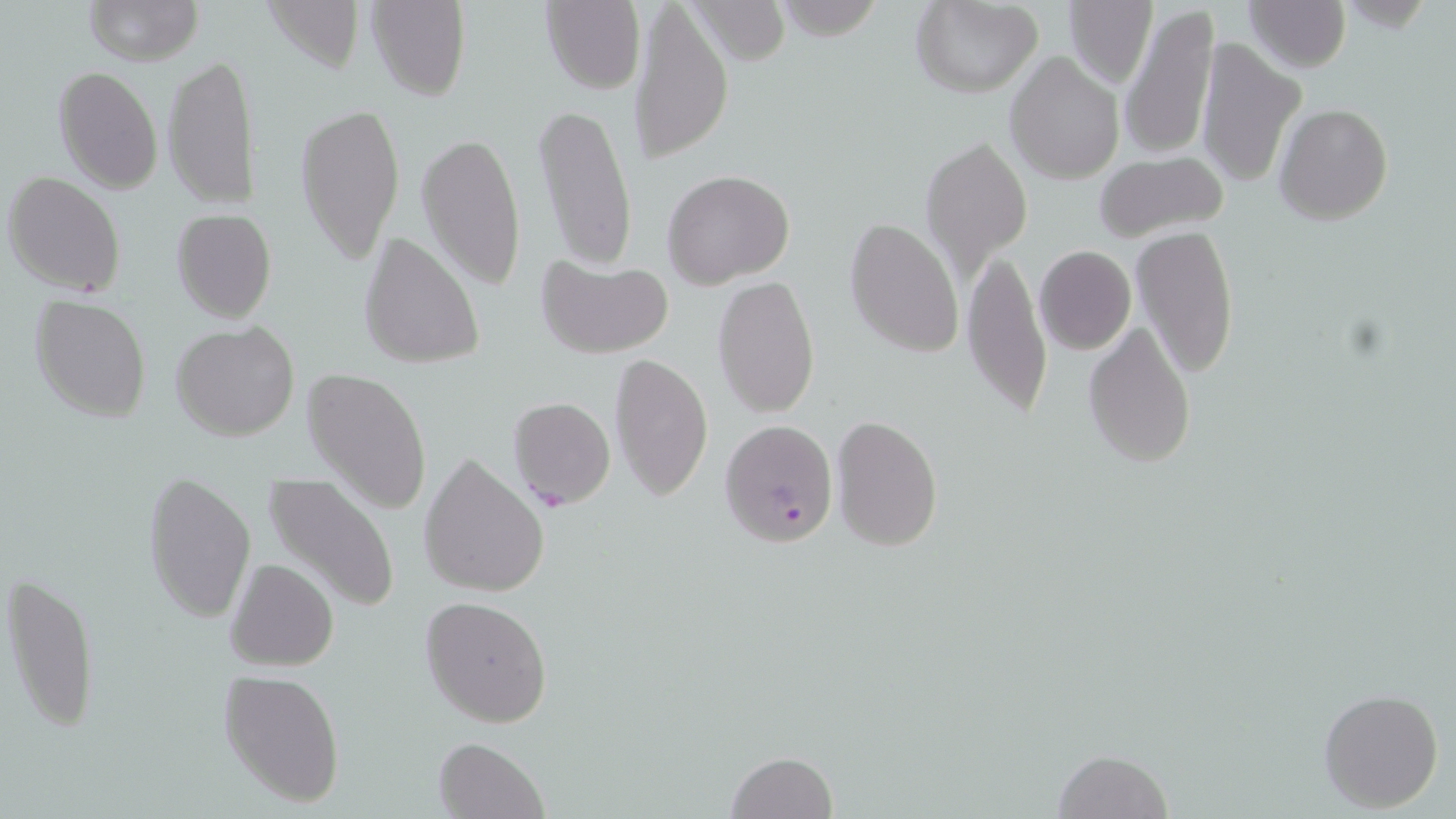
Summary:
  - Coordinate format: approximate bounding boxes as [x1, y1, x2, y2] in pixels
  - Plasmodium falciparum-infected red blood cell locations: [719, 419, 840, 549]
  - Uninfected red blood cell locations: [83, 0, 203, 66], [366, 0, 471, 101], [1063, 0, 1157, 89], [1243, 0, 1351, 72], [541, 1, 645, 95], [910, 1, 1044, 98], [1118, 2, 1219, 160], [630, 3, 734, 165], [1195, 38, 1306, 187], [1005, 50, 1125, 185], [163, 52, 261, 209], [54, 64, 162, 193], [295, 102, 405, 266], [532, 102, 638, 272], [1275, 104, 1393, 225], [415, 129, 528, 291], [922, 133, 1032, 285], [1092, 152, 1231, 246], [662, 170, 796, 288], [5, 171, 125, 296], [171, 208, 277, 323], [845, 217, 963, 358], [1131, 223, 1240, 379], [358, 230, 485, 371], [1034, 246, 1136, 354], [961, 247, 1052, 421], [535, 254, 674, 359], [712, 273, 820, 419], [31, 295, 152, 422], [171, 320, 299, 441], [1082, 321, 1196, 470], [610, 353, 713, 501], [303, 368, 433, 515], [507, 396, 616, 511], [831, 414, 943, 550], [418, 456, 550, 598], [142, 471, 257, 625], [262, 471, 400, 614], [227, 557, 339, 672], [5, 569, 99, 740], [421, 596, 552, 727], [219, 670, 346, 807], [1317, 687, 1444, 814], [433, 735, 549, 819], [1052, 748, 1175, 819], [724, 750, 838, 819]
  - Slide-level diagnosis: Plasmodium falciparum
  - Stain: May-Grünwald-Giemsa
  - Modality: light microscopy
  - Field of view: one of a larger specimen
  - Magnification: 1000x
  - Preparation: thin blood film
  - Image size: 1456×819 pixels